Comment on the morphology of the red blood cells.
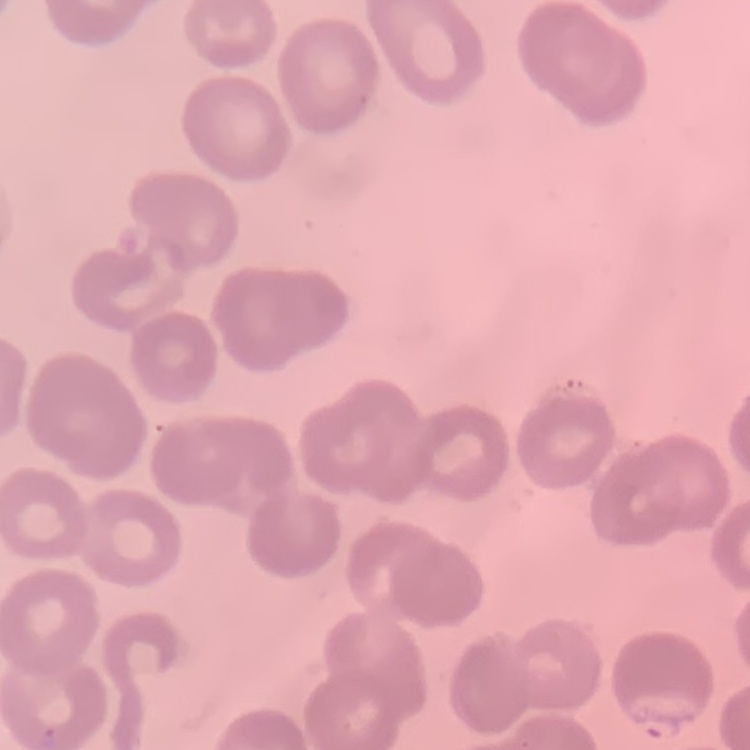
No rouleaux formation.

Summary:
  - Stain: Field's or Giemsa
  - Image type: square crop of a larger photomicrograph
  - Preparation: thin blood film